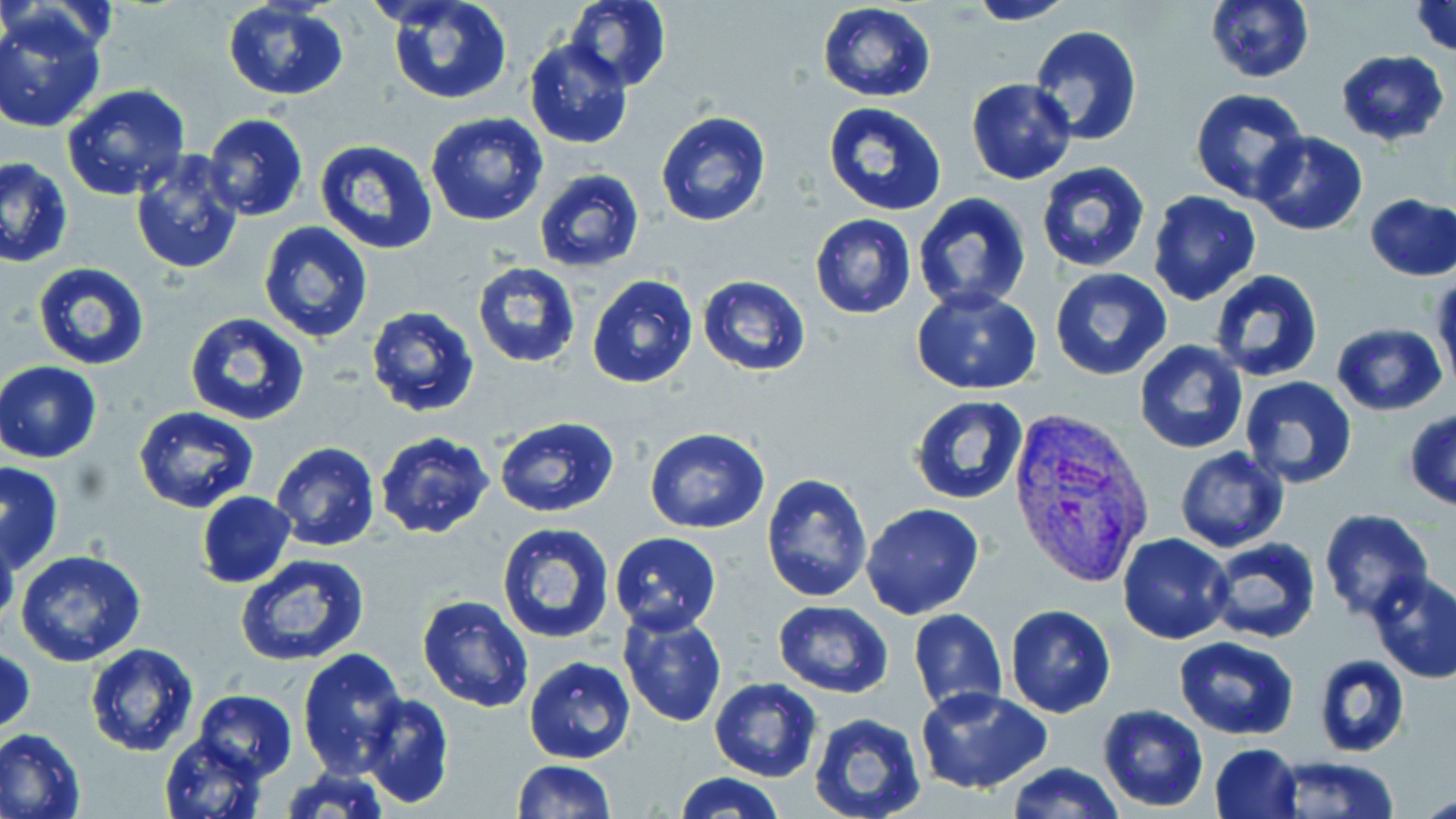

slide_level_diagnosis: Plasmodium vivax
image_size: 1456×819 pixels
plasmodium_vivax_infected_red_blood_cell_locations: 'approximate bounding boxes as [x1, y1, x2, y2] in pixels: [1006, 405, 1159, 593]'
uninfected_red_blood_cell_locations: 'approximate bounding boxes as [x1, y1, x2, y2] in pixels: [386, 0, 510, 106], [563, 0, 672, 91], [1205, 0, 1314, 84], [964, 1, 1079, 24], [1407, 1, 1456, 58], [220, 2, 350, 102], [817, 3, 937, 103], [0, 6, 107, 134], [1029, 26, 1145, 146], [523, 39, 632, 150], [1334, 49, 1450, 146], [966, 78, 1076, 184], [62, 84, 192, 202], [1189, 88, 1310, 206], [823, 101, 948, 216], [655, 110, 772, 229], [425, 111, 548, 227], [203, 112, 309, 222], [1252, 131, 1367, 235], [314, 141, 438, 256], [130, 152, 245, 276], [0, 158, 73, 268], [1036, 160, 1150, 273], [536, 169, 644, 273], [1148, 190, 1261, 305], [913, 193, 1034, 314], [1365, 193, 1456, 282], [809, 214, 916, 319], [257, 221, 373, 344], [33, 260, 150, 370], [471, 261, 581, 369], [1050, 269, 1173, 382], [1208, 270, 1326, 384], [586, 274, 699, 390], [697, 274, 811, 376], [1432, 275, 1456, 393], [912, 288, 1041, 394], [365, 306, 481, 420], [184, 312, 311, 427], [1332, 324, 1447, 414], [1134, 340, 1248, 455], [0, 360, 102, 464], [1239, 376, 1359, 490], [909, 395, 1029, 503], [134, 406, 258, 513], [1405, 408, 1456, 511], [493, 417, 620, 519], [644, 428, 770, 533], [373, 431, 496, 539], [270, 442, 379, 552], [1174, 446, 1290, 552], [1, 461, 65, 573], [761, 472, 873, 602], [197, 491, 296, 587], [860, 502, 985, 620], [1317, 508, 1434, 620], [496, 521, 616, 642], [0, 524, 19, 632], [609, 531, 721, 634], [1117, 533, 1234, 643], [1204, 536, 1323, 646], [15, 549, 147, 665], [236, 554, 369, 669], [1366, 571, 1456, 684], [417, 592, 535, 713], [770, 601, 894, 698], [1004, 604, 1116, 717], [908, 609, 1008, 713], [619, 610, 728, 729], [1173, 636, 1298, 740], [84, 642, 198, 756], [1, 646, 35, 739], [296, 647, 406, 776], [1313, 655, 1408, 758], [523, 656, 635, 765], [710, 677, 821, 782], [916, 686, 1052, 795], [191, 690, 298, 781], [359, 693, 454, 809], [1097, 704, 1209, 811], [808, 713, 927, 819], [0, 726, 86, 819], [160, 735, 266, 819], [1210, 742, 1303, 819], [1270, 755, 1400, 818], [511, 759, 615, 818], [1004, 761, 1126, 818], [280, 766, 391, 819], [673, 771, 785, 819], [1417, 790, 1456, 817]'
modality: light microscopy
preparation: thin blood film
magnification: 1000x
stain: May-Grünwald-Giemsa
field_of_view: single